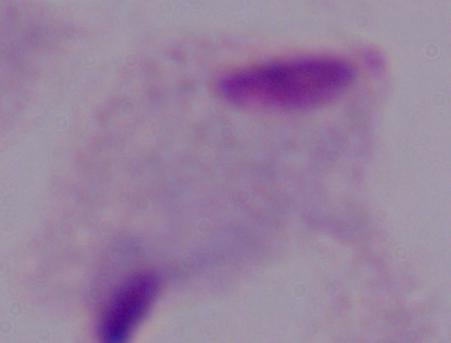
identification = trichomonad
magnification = 1000x
modality = photomicrograph